Identify the blood parasite species.
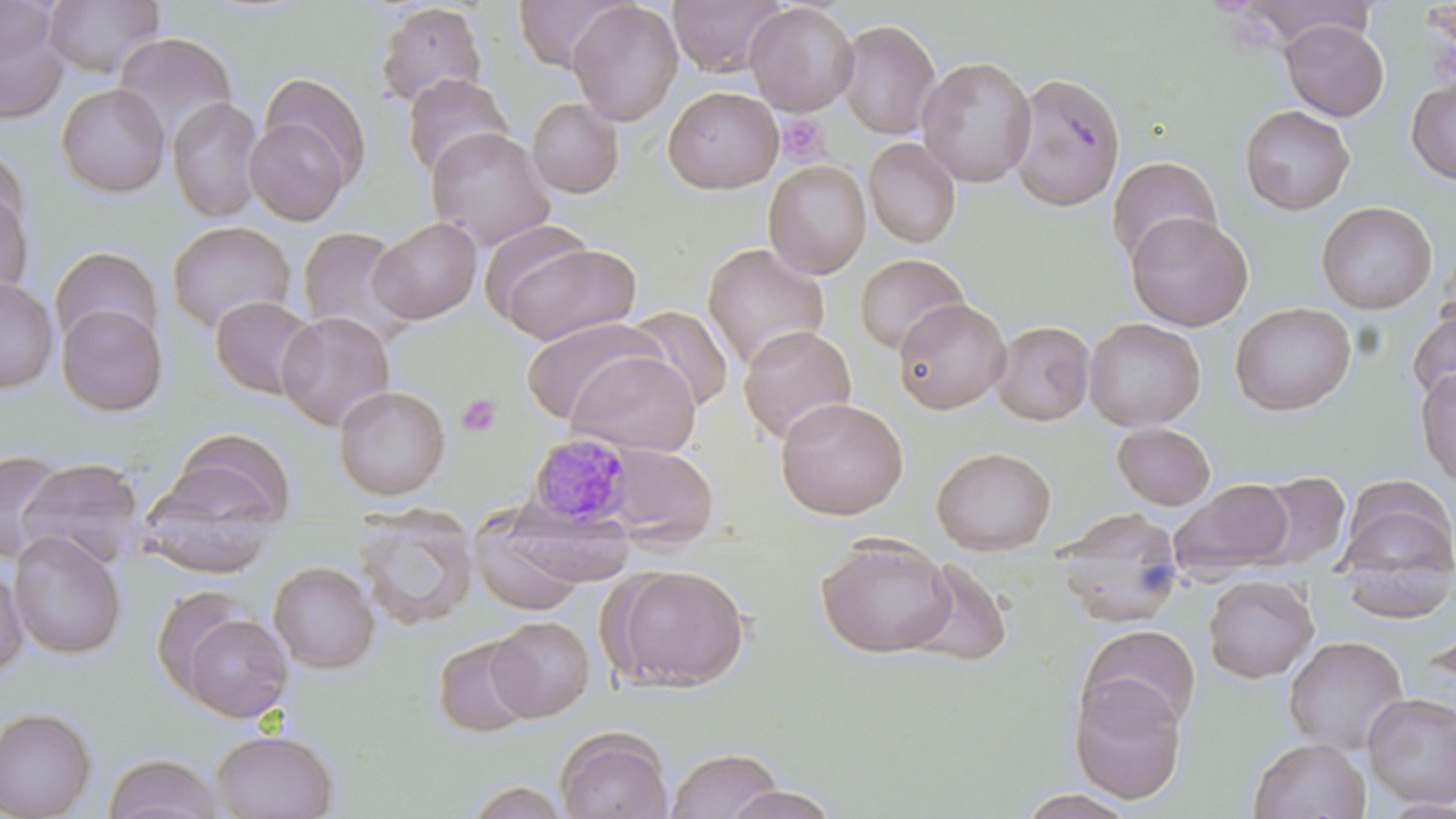
Plasmodium malariae.

Summary:
  - Coordinate format: approximate bounding boxes as (x1,y1)-(x2,y2) corner pairs in pixels
  - Platelet locations: (776,113)-(829,165), (456,393)-(501,438)
  - Plasmodium malariae-infected red blood cell locations: (526,433)-(636,528)
  - Uninfected red blood cell locations: (41,0)-(166,80), (512,0)-(630,73), (668,0)-(787,78), (1236,0)-(1375,48), (567,1)-(683,126), (375,2)-(488,109), (744,2)-(859,117), (0,4)-(70,123), (835,19)-(941,140), (1280,19)-(1389,122), (111,33)-(238,147), (916,55)-(1037,187), (1008,71)-(1127,212), (259,72)-(373,189), (401,73)-(514,180), (1406,76)-(1456,185), (56,82)-(170,198), (663,86)-(783,194), (167,96)-(266,225), (527,97)-(624,198), (1239,105)-(1355,215), (243,116)-(351,226), (426,127)-(555,250), (863,137)-(962,249), (0,147)-(31,244), (1106,156)-(1221,265), (763,160)-(871,279), (0,186)-(34,304), (1316,201)-(1437,314), (1125,211)-(1253,331), (368,217)-(482,324), (166,221)-(296,335), (297,225)-(415,345), (493,240)-(643,345), (702,242)-(830,372), (50,246)-(162,350), (854,253)-(970,355), (0,278)-(59,394), (211,295)-(319,400), (892,298)-(1011,414), (1230,302)-(1356,415), (56,303)-(168,417), (622,305)-(734,413), (1407,307)-(1456,408), (276,311)-(395,432), (520,317)-(666,425), (1084,317)-(1205,431), (990,320)-(1095,426), (738,324)-(857,444), (566,350)-(702,457), (1414,368)-(1456,487), (333,385)-(451,500), (775,396)-(908,520), (1111,423)-(1216,510), (163,428)-(297,530), (597,441)-(719,548), (931,446)-(1056,555), (0,449)-(67,563), (17,457)-(148,568), (1251,472)-(1350,572), (137,476)-(278,578), (1170,479)-(1295,578), (1336,481)-(1456,605), (469,505)-(590,616), (353,507)-(479,631), (1054,510)-(1186,630), (7,529)-(128,660), (817,536)-(957,658), (906,558)-(1013,668), (268,561)-(380,673), (610,564)-(750,691), (0,565)-(29,681), (1203,574)-(1319,683), (152,585)-(258,701), (177,611)-(294,723), (1424,614)-(1456,695), (486,615)-(595,722), (1077,624)-(1201,733), (433,635)-(535,739), (1283,635)-(1409,756), (1068,674)-(1188,805), (1362,692)-(1456,809), (0,706)-(97,818), (555,726)-(672,819), (211,728)-(339,819), (1247,737)-(1372,819), (665,746)-(786,819), (103,753)-(224,819), (461,780)-(574,818), (722,785)-(841,819), (1012,790)-(1142,819)
  - Image size: 1456×819 pixels
  - Magnification: 1000x
  - Modality: optical microscopy
  - Field of view: one of a larger specimen
  - Stain: May-Grünwald-Giemsa
  - Preparation: thin blood smear